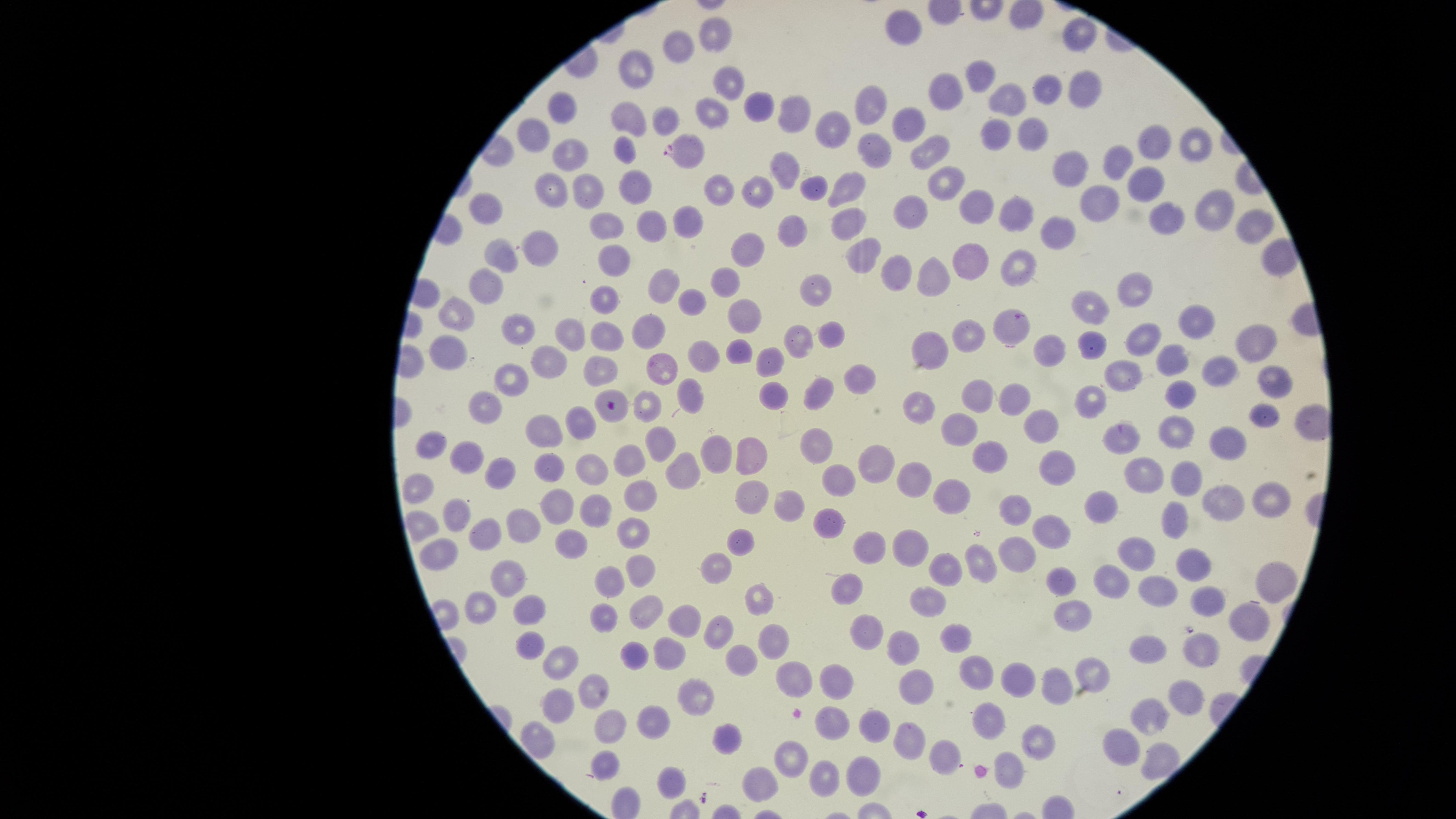

parasitized red blood cells = approximate marker points as (x, y) in pixels: (687, 150), (1016, 325)
visible region = circular
stain = Giemsa
capture = smartphone photograph through the microscope eyepiece
image size = 1456×819 pixels
preparation = thin blood smear
presence = malaria parasites identified
uninfected red blood cells = approximate marker points as (x, y) in pixels: (902, 24), (1080, 35), (715, 36), (684, 47), (642, 68), (980, 81), (728, 82), (1084, 84), (1046, 88), (948, 91), (872, 104), (570, 105), (1008, 105), (761, 108), (797, 113), (631, 114), (711, 116), (668, 120), (909, 122), (833, 133), (1029, 134), (529, 136), (994, 136), (1149, 140), (1195, 141), (879, 147), (926, 149), (561, 150), (626, 150), (1119, 164), (1076, 167), (786, 169), (1149, 184), (552, 185), (637, 185), (851, 185), (943, 186), (722, 188), (588, 190), (810, 190), (763, 194), (1090, 201), (1209, 206), (982, 208), (487, 214), (905, 214), (1017, 215), (607, 222), (687, 222), (1164, 223), (651, 225), (853, 225), (1254, 229), (788, 230), (1058, 230), (544, 248), (751, 253), (865, 254), (614, 257), (500, 260), (1023, 263), (979, 265), (899, 276), (722, 281), (926, 281), (485, 285), (1141, 286), (818, 287), (659, 288), (603, 300), (689, 300), (1094, 308), (461, 313), (1197, 316), (744, 319), (519, 327), (645, 330), (828, 332), (606, 335), (565, 337), (1249, 337), (797, 338), (970, 338), (1141, 338), (1089, 349), (922, 353), (702, 354), (1042, 354), (737, 355), (1169, 356), (447, 361), (605, 361), (771, 361), (547, 363), (664, 363), (1217, 367), (848, 372), (1124, 376), (510, 381), (1270, 383), (1176, 388), (684, 389), (979, 394), (818, 395), (1011, 396), (771, 397), (1097, 398), (920, 407), (640, 409), (614, 414), (485, 416), (1262, 419), (1047, 421), (543, 422), (960, 427), (578, 429), (1175, 432), (1123, 434), (1221, 440), (660, 445), (818, 448), (427, 451), (715, 454), (753, 457), (988, 457), (877, 459), (464, 460), (628, 460), (1057, 461), (551, 466), (590, 468), (498, 469), (684, 472), (916, 481), (1147, 481), (1187, 481), (834, 482), (418, 486), (638, 497), (955, 498), (788, 505), (1100, 505), (1220, 505), (1263, 505), (751, 506), (560, 508), (1022, 511), (594, 512), (453, 513), (1175, 519), (419, 521), (631, 522), (830, 522), (522, 529), (1057, 531), (480, 534), (570, 540), (740, 544), (437, 545), (873, 545), (906, 549), (1018, 555), (1133, 558), (982, 562), (716, 565), (1193, 566), (941, 568), (512, 571), (1271, 577), (637, 580), (1063, 581), (606, 582), (1117, 585), (847, 592), (761, 594), (1164, 594), (1203, 594), (929, 600), (481, 604), (528, 610), (1072, 610), (647, 611), (1248, 613), (598, 617), (680, 623), (875, 625), (723, 627), (772, 634), (957, 637), (528, 645), (909, 648), (1201, 648), (1149, 651), (636, 654), (666, 656), (561, 658), (735, 660), (1090, 667), (976, 675), (841, 679), (789, 680), (916, 683), (1018, 683), (1055, 684), (594, 692), (1185, 696), (701, 699), (554, 707), (1155, 720), (829, 721), (656, 723), (993, 725), (870, 726), (607, 728), (725, 737), (907, 738), (1036, 747), (941, 755), (1125, 755), (785, 761), (1156, 761), (606, 767), (862, 774), (1005, 775), (821, 778), (666, 780), (760, 788)
field of view = single
species = Plasmodium falciparum